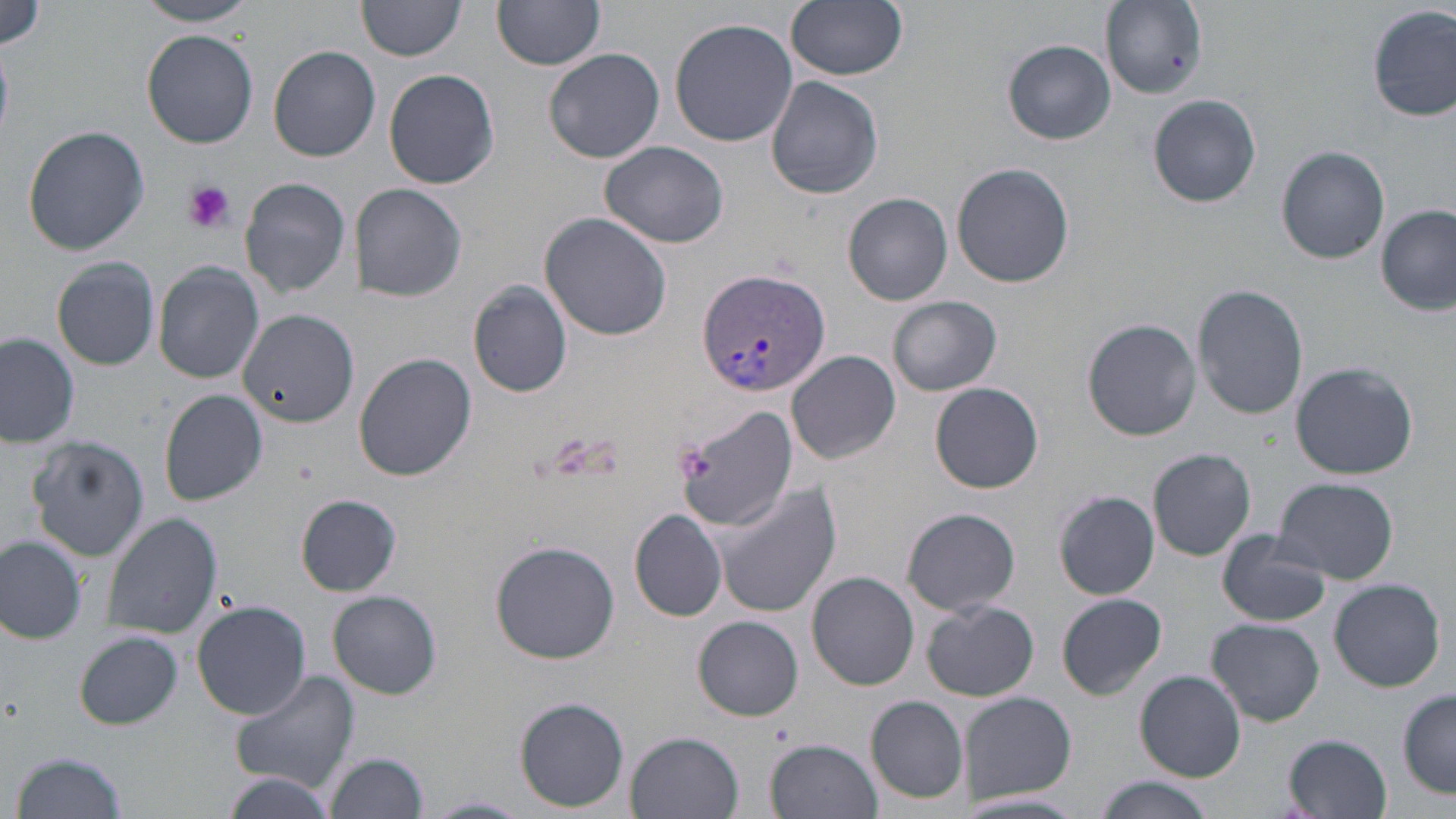
slide_level_diagnosis: Plasmodium vivax
preparation: thin blood smear
plasmodium_vivax_infected_red_blood_cell_locations: 'approximate bounding boxes as named x1/y1/x2/y2 corners in pixels: (x1=697, y1=266, x2=830, y2=396)'
platelet_locations: 'approximate bounding boxes as named x1/y1/x2/y2 corners in pixels: (x1=181, y1=180, x2=236, y2=234), (x1=675, y1=442, x2=711, y2=486)'
image_size: 1456×819 pixels
stain: May-Grünwald-Giemsa
field_of_view: single
uninfected_red_blood_cell_locations: 'approximate bounding boxes as named x1/y1/x2/y2 corners in pixels: (x1=133, y1=0, x2=264, y2=27), (x1=785, y1=0, x2=909, y2=81), (x1=0, y1=1, x2=46, y2=55), (x1=356, y1=2, x2=465, y2=63), (x1=495, y1=2, x2=604, y2=71), (x1=1104, y1=2, x2=1206, y2=99), (x1=1367, y1=6, x2=1454, y2=123), (x1=670, y1=17, x2=798, y2=146), (x1=142, y1=27, x2=260, y2=148), (x1=1002, y1=40, x2=1116, y2=144), (x1=270, y1=46, x2=381, y2=162), (x1=544, y1=47, x2=664, y2=164), (x1=383, y1=68, x2=500, y2=188), (x1=766, y1=75, x2=884, y2=199), (x1=1147, y1=95, x2=1261, y2=208), (x1=22, y1=126, x2=150, y2=256), (x1=599, y1=140, x2=730, y2=250), (x1=1278, y1=145, x2=1389, y2=264), (x1=951, y1=163, x2=1075, y2=287), (x1=238, y1=176, x2=350, y2=298), (x1=354, y1=182, x2=467, y2=302), (x1=844, y1=192, x2=952, y2=306), (x1=1376, y1=205, x2=1453, y2=314), (x1=540, y1=211, x2=672, y2=341), (x1=52, y1=258, x2=159, y2=371), (x1=153, y1=262, x2=264, y2=383), (x1=468, y1=280, x2=574, y2=398), (x1=1192, y1=283, x2=1310, y2=419), (x1=888, y1=294, x2=1001, y2=396), (x1=237, y1=308, x2=358, y2=427), (x1=1083, y1=320, x2=1200, y2=440), (x1=1, y1=332, x2=79, y2=448), (x1=788, y1=350, x2=901, y2=465), (x1=354, y1=353, x2=476, y2=480), (x1=1290, y1=361, x2=1419, y2=479), (x1=930, y1=382, x2=1044, y2=494), (x1=160, y1=389, x2=268, y2=506), (x1=675, y1=406, x2=799, y2=530), (x1=26, y1=434, x2=149, y2=562), (x1=1148, y1=448, x2=1257, y2=561), (x1=1275, y1=477, x2=1399, y2=584), (x1=709, y1=483, x2=842, y2=618), (x1=1054, y1=491, x2=1161, y2=600), (x1=297, y1=495, x2=401, y2=595), (x1=901, y1=507, x2=1021, y2=616), (x1=630, y1=509, x2=728, y2=622), (x1=101, y1=512, x2=222, y2=640), (x1=1217, y1=530, x2=1330, y2=627), (x1=0, y1=536, x2=86, y2=644), (x1=490, y1=540, x2=621, y2=664), (x1=808, y1=572, x2=918, y2=691), (x1=1329, y1=578, x2=1445, y2=692), (x1=328, y1=589, x2=441, y2=699), (x1=1058, y1=593, x2=1167, y2=699), (x1=922, y1=599, x2=1040, y2=702), (x1=192, y1=601, x2=311, y2=720), (x1=694, y1=616, x2=804, y2=719), (x1=1210, y1=617, x2=1324, y2=725), (x1=76, y1=632, x2=182, y2=729), (x1=227, y1=670, x2=360, y2=796), (x1=1135, y1=670, x2=1247, y2=780), (x1=1398, y1=691, x2=1456, y2=796), (x1=967, y1=692, x2=1078, y2=803), (x1=866, y1=696, x2=967, y2=804), (x1=514, y1=698, x2=628, y2=811), (x1=628, y1=731, x2=744, y2=818), (x1=1285, y1=733, x2=1393, y2=817), (x1=767, y1=737, x2=883, y2=819), (x1=11, y1=750, x2=131, y2=819), (x1=324, y1=751, x2=428, y2=819), (x1=223, y1=770, x2=334, y2=817), (x1=1093, y1=777, x2=1217, y2=819), (x1=424, y1=795, x2=527, y2=818)'
modality: light microscopy
magnification: 1000x